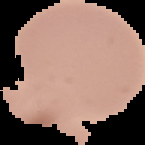

preparation = thin blood film
image type = segmented cell region on a black background
image size = 145×145 pixels
result = no Plasmodium parasites detected